Report the malaria status of this cell.
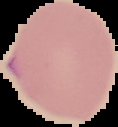
Parasitized.

Summary:
  - Image size: 118×127 pixels
  - Image type: segmented cell region with the area outside set to black
  - Preparation: thin blood smear